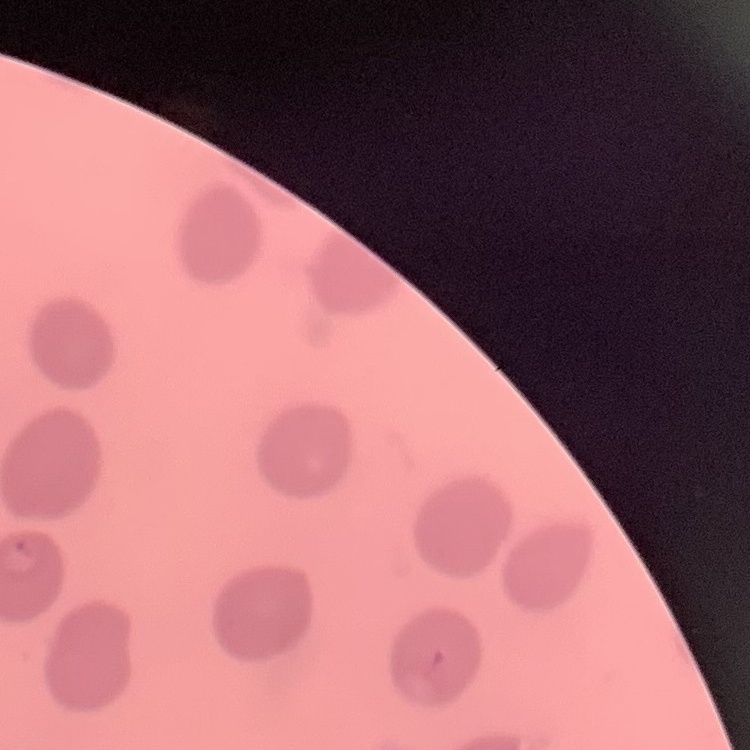
Summary:
  - Red blood cell morphology: no rouleaux formation
  - Image type: one tile cut from a larger photomicrograph
  - Preparation: thin blood smear
  - Stain: Field's or Giemsa